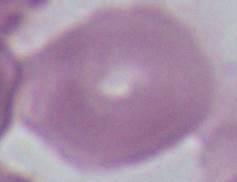 Captured at 1000x magnification. Photomicrograph. A red blood cell is shown.